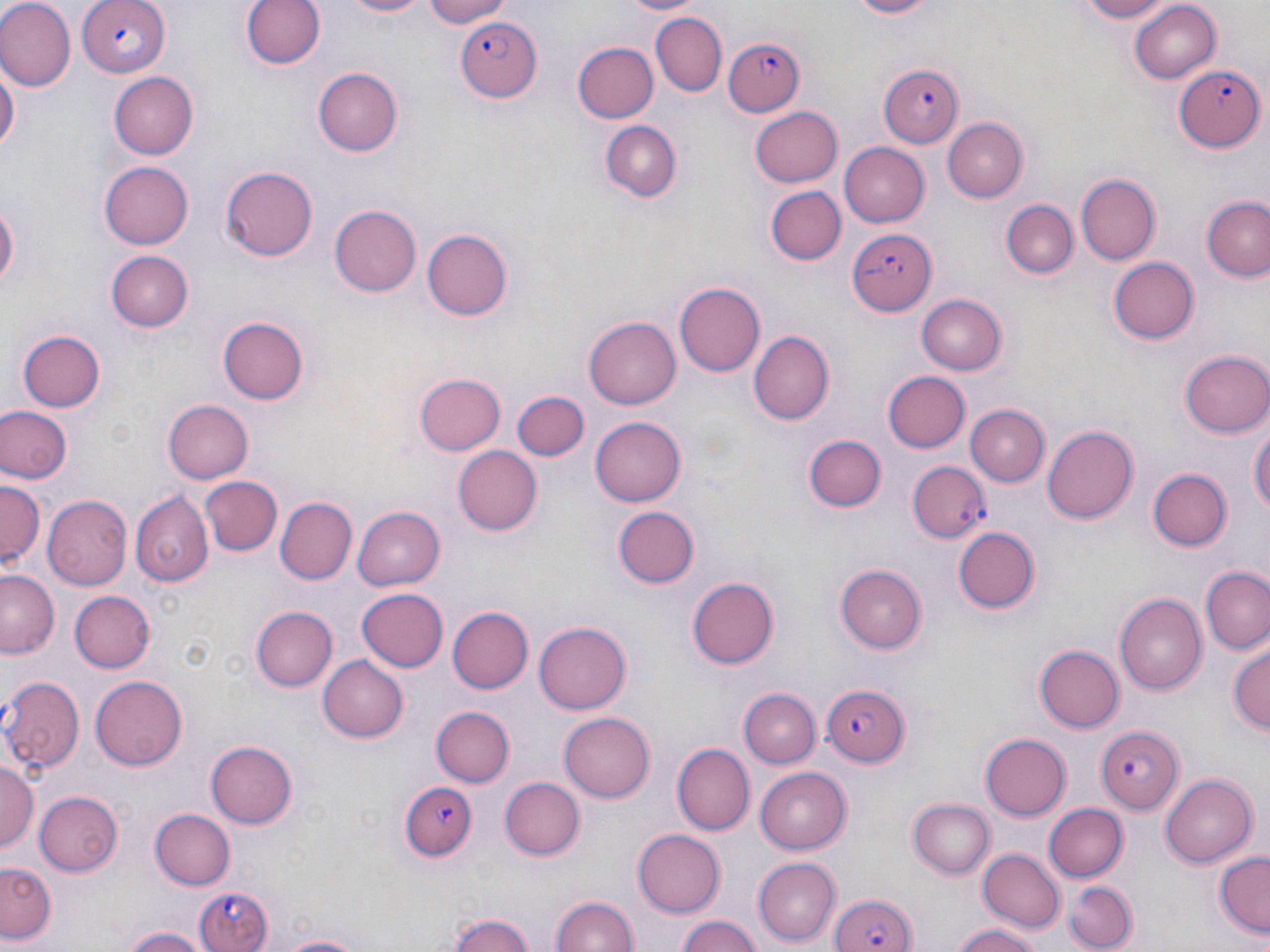

Approximate bounding boxes as named x1/y1/x2/y2 corners in pixels. Plasmodium falciparum-infected red blood cell locations: (x1=76, y1=0, x2=170, y2=75), (x1=455, y1=15, x2=542, y2=103), (x1=725, y1=38, x2=806, y2=117), (x1=1173, y1=65, x2=1264, y2=151), (x1=879, y1=66, x2=962, y2=147), (x1=847, y1=226, x2=936, y2=318), (x1=907, y1=463, x2=989, y2=542), (x1=819, y1=682, x2=910, y2=765), (x1=1094, y1=727, x2=1183, y2=814), (x1=397, y1=780, x2=479, y2=863), (x1=193, y1=884, x2=271, y2=952), (x1=829, y1=890, x2=916, y2=952). Uninfected red blood cell locations: (x1=0, y1=0, x2=75, y2=89), (x1=237, y1=0, x2=327, y2=73), (x1=338, y1=0, x2=435, y2=19), (x1=417, y1=0, x2=517, y2=27), (x1=615, y1=0, x2=704, y2=16), (x1=839, y1=0, x2=949, y2=20), (x1=1070, y1=0, x2=1175, y2=23), (x1=1126, y1=2, x2=1222, y2=84), (x1=651, y1=12, x2=726, y2=97), (x1=573, y1=44, x2=659, y2=123), (x1=0, y1=58, x2=18, y2=160), (x1=312, y1=67, x2=401, y2=156), (x1=108, y1=71, x2=198, y2=161), (x1=751, y1=104, x2=843, y2=186), (x1=942, y1=118, x2=1029, y2=205), (x1=599, y1=120, x2=683, y2=203), (x1=837, y1=142, x2=930, y2=226), (x1=100, y1=162, x2=193, y2=248), (x1=223, y1=165, x2=319, y2=261), (x1=1075, y1=175, x2=1160, y2=265), (x1=766, y1=186, x2=846, y2=265), (x1=1201, y1=191, x2=1270, y2=285), (x1=0, y1=192, x2=19, y2=298), (x1=1000, y1=199, x2=1078, y2=278), (x1=328, y1=205, x2=421, y2=297), (x1=420, y1=226, x2=515, y2=322), (x1=106, y1=251, x2=194, y2=331), (x1=1106, y1=256, x2=1198, y2=344), (x1=675, y1=282, x2=765, y2=377), (x1=915, y1=294, x2=1006, y2=375), (x1=583, y1=314, x2=680, y2=407), (x1=216, y1=316, x2=309, y2=406), (x1=17, y1=328, x2=105, y2=412), (x1=748, y1=332, x2=832, y2=424), (x1=1180, y1=350, x2=1270, y2=439), (x1=882, y1=371, x2=969, y2=453), (x1=415, y1=373, x2=504, y2=456), (x1=511, y1=390, x2=588, y2=461), (x1=163, y1=400, x2=254, y2=482), (x1=1, y1=404, x2=73, y2=484), (x1=965, y1=404, x2=1051, y2=486), (x1=591, y1=417, x2=686, y2=507), (x1=1250, y1=418, x2=1269, y2=528), (x1=1042, y1=425, x2=1138, y2=524), (x1=805, y1=433, x2=886, y2=512), (x1=453, y1=443, x2=542, y2=533), (x1=1148, y1=469, x2=1230, y2=551), (x1=203, y1=477, x2=280, y2=555), (x1=0, y1=478, x2=44, y2=565), (x1=132, y1=492, x2=214, y2=587), (x1=44, y1=496, x2=132, y2=590), (x1=277, y1=497, x2=356, y2=583), (x1=355, y1=506, x2=447, y2=591), (x1=614, y1=506, x2=700, y2=589), (x1=952, y1=526, x2=1041, y2=614), (x1=836, y1=564, x2=928, y2=653), (x1=1202, y1=568, x2=1270, y2=654), (x1=1, y1=569, x2=58, y2=657), (x1=686, y1=574, x2=780, y2=669), (x1=355, y1=587, x2=450, y2=673), (x1=1117, y1=590, x2=1209, y2=694), (x1=68, y1=591, x2=156, y2=672), (x1=447, y1=604, x2=534, y2=694), (x1=250, y1=605, x2=336, y2=692), (x1=535, y1=622, x2=631, y2=714), (x1=1227, y1=642, x2=1268, y2=738), (x1=1037, y1=643, x2=1127, y2=731), (x1=318, y1=656, x2=409, y2=743), (x1=91, y1=675, x2=187, y2=770), (x1=0, y1=676, x2=86, y2=772), (x1=740, y1=687, x2=821, y2=766), (x1=429, y1=706, x2=513, y2=788), (x1=557, y1=712, x2=655, y2=803), (x1=978, y1=733, x2=1070, y2=821), (x1=203, y1=737, x2=298, y2=829), (x1=672, y1=744, x2=754, y2=834), (x1=0, y1=758, x2=38, y2=856), (x1=755, y1=765, x2=852, y2=850), (x1=1160, y1=772, x2=1257, y2=867), (x1=501, y1=776, x2=586, y2=861), (x1=34, y1=790, x2=122, y2=874), (x1=907, y1=797, x2=994, y2=879), (x1=1043, y1=803, x2=1127, y2=881), (x1=150, y1=808, x2=235, y2=888), (x1=1058, y1=809, x2=1133, y2=952), (x1=630, y1=829, x2=723, y2=917), (x1=977, y1=848, x2=1063, y2=932), (x1=1213, y1=851, x2=1269, y2=937), (x1=753, y1=857, x2=840, y2=945), (x1=2, y1=861, x2=59, y2=944), (x1=1065, y1=878, x2=1137, y2=951), (x1=548, y1=893, x2=640, y2=952), (x1=444, y1=912, x2=540, y2=952), (x1=675, y1=915, x2=767, y2=952), (x1=949, y1=924, x2=1043, y2=952), (x1=120, y1=926, x2=215, y2=952), (x1=273, y1=934, x2=366, y2=952). Slide-level diagnosis: Plasmodium falciparum. Image is 1270×952 pixels. May-Grünwald-Giemsa stain. 1000x magnification. Optical microscopy. Thin blood smear. Single field of view.